Name the cell type shown.
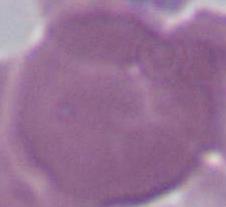
An erythrocyte.

Captured at 1000x magnification. Micrograph.